Describe the morphology of the red blood cells.
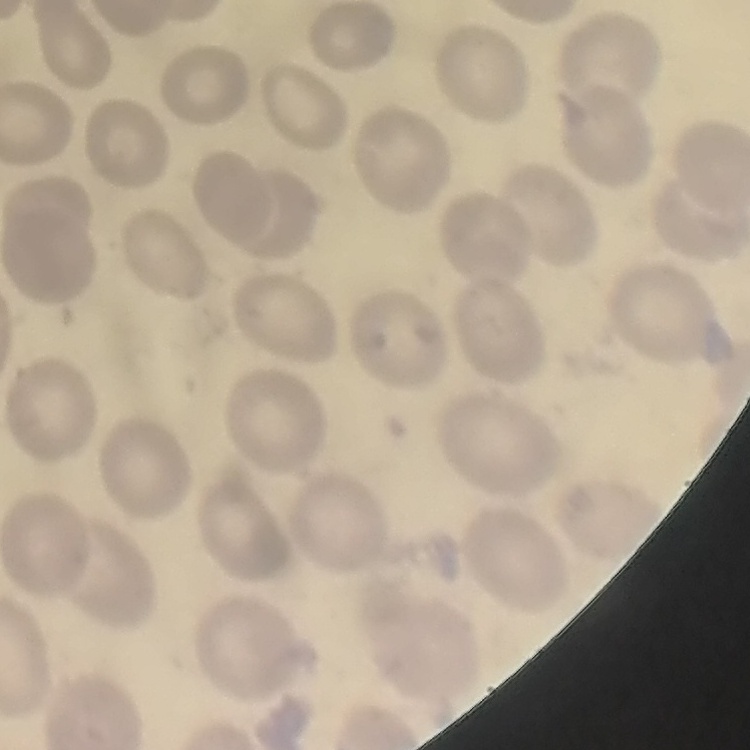
They show no rouleaux formation.

Summary:
  - Preparation: thin blood film
  - Stain: Field's or Giemsa
  - Image type: one tile cut from a larger photomicrograph